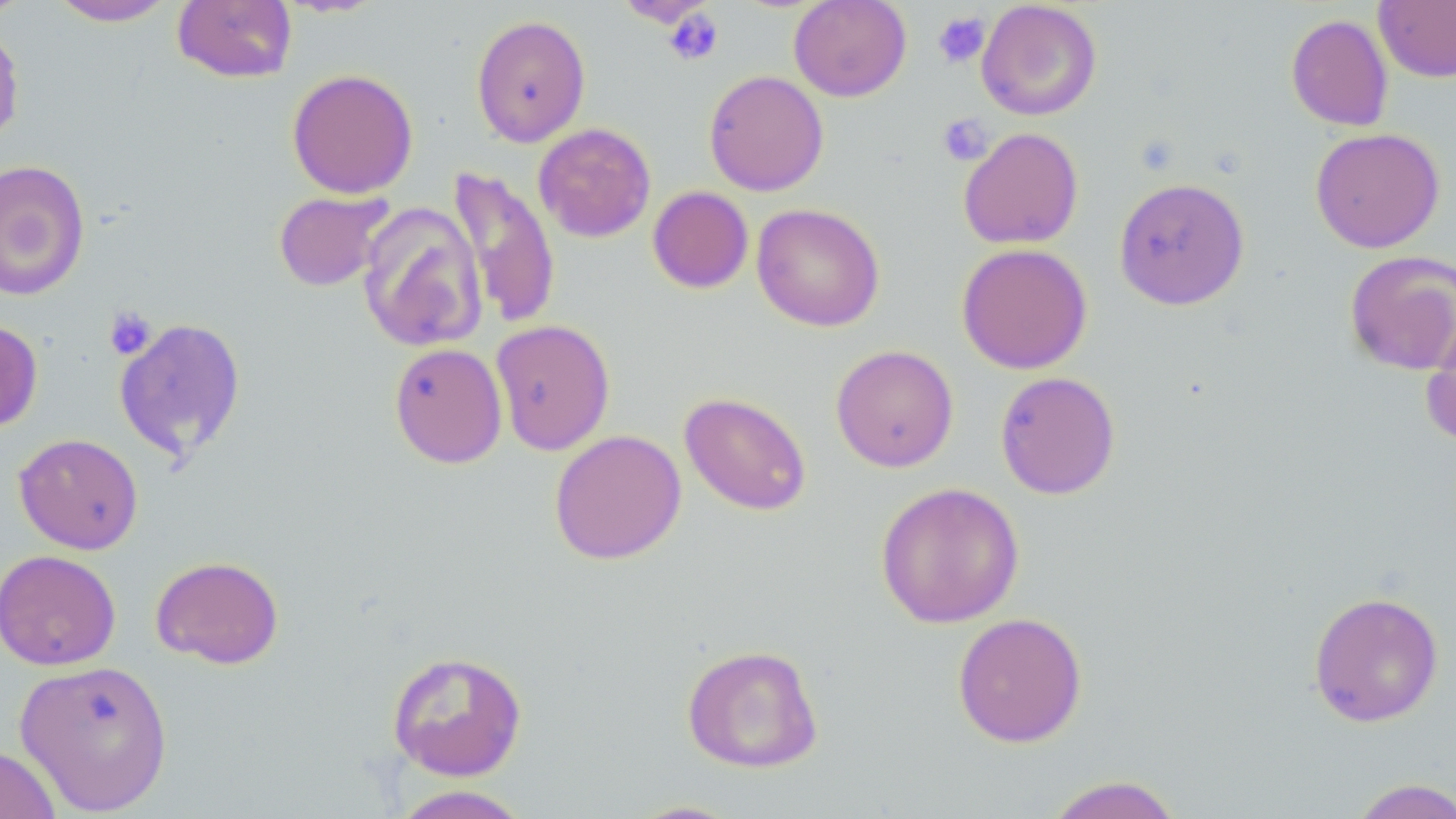 Approximate bounding boxes as (x1,y1)-(x2,y2) corner pairs in pixels. Platelet locations: (663,8)-(724,66), (933,11)-(990,68), (937,114)-(993,166), (104,308)-(157,360). Uninfected red blood cell locations: (0,0)-(31,23), (49,0)-(177,26), (614,0)-(717,27), (788,0)-(912,102), (173,1)-(297,84), (976,1)-(1102,121), (1374,1)-(1456,82), (1285,13)-(1393,132), (470,14)-(591,147), (0,21)-(25,148), (287,68)-(419,199), (703,70)-(829,196), (533,123)-(656,243), (958,127)-(1084,250), (1310,127)-(1445,253), (0,159)-(91,301), (447,167)-(562,330), (1113,177)-(1250,310), (647,186)-(754,294), (273,189)-(393,292), (357,202)-(487,353), (751,203)-(885,331), (955,243)-(1093,374), (1344,250)-(1456,376), (1419,314)-(1456,450), (114,317)-(247,462), (0,319)-(43,432), (490,319)-(615,455), (389,342)-(507,469), (830,344)-(959,472), (995,371)-(1121,499), (679,391)-(812,516), (549,429)-(687,565), (14,433)-(144,554), (874,482)-(1025,629), (0,549)-(121,671), (150,555)-(285,670), (1308,591)-(1445,727), (951,611)-(1088,748), (681,644)-(824,773), (386,649)-(529,782), (14,658)-(174,814), (0,745)-(61,819), (1042,775)-(1185,819), (1346,778)-(1456,819), (389,785)-(533,819), (625,799)-(746,818). Slide-level diagnosis: no evidence of blood parasites. Single field of view. Optical microscopy. Thin blood smear. Image is 1456×819 pixels. May-Grünwald-Giemsa-stained preparation. Captured at 1000x magnification.